Outline each blood parasite and name the species.
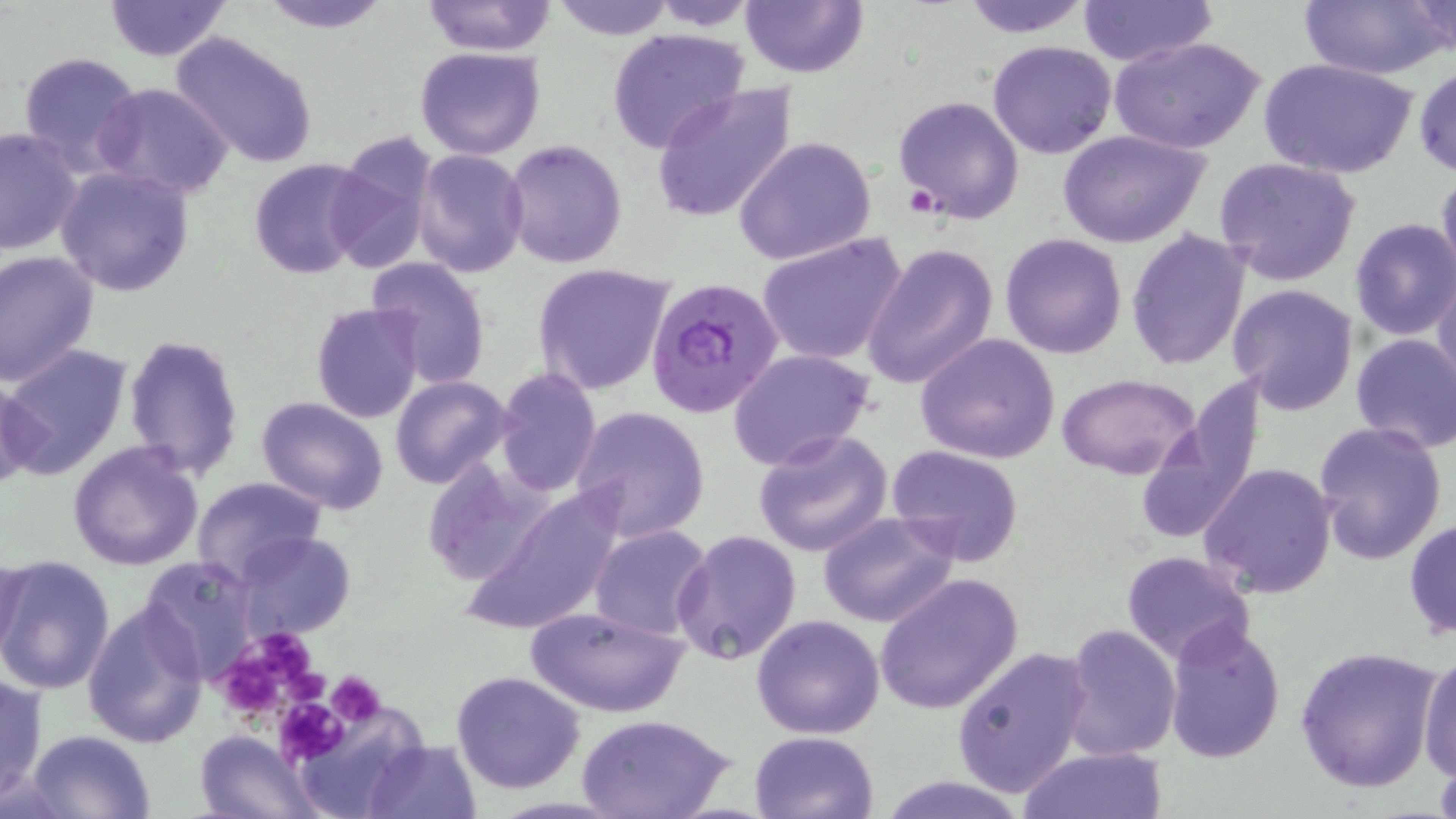

Approximate bounding boxes as [x1, y1, x2, y2] in pixels.
Plasmodium falciparum-infected red blood cells: [646, 277, 786, 418].
No Plasmodium ovale, Plasmodium malariae, Plasmodium vivax, Babesia divergens, or Trypanosoma brucei observed.

{
  "slide_level_diagnosis": "Plasmodium falciparum",
  "modality": "optical microscopy",
  "preparation": "thin blood film",
  "stain": "May-Grünwald-Giemsa",
  "magnification": "1000x",
  "field_of_view": "single",
  "platelet_locations": "approximate bounding boxes as [x1, y1, x2, y2] in pixels: [253, 631, 319, 684], [216, 654, 294, 719], [284, 666, 322, 711], [327, 671, 385, 724], [276, 696, 348, 764]",
  "image_size": "1456×819 pixels",
  "uninfected_red_blood_cell_locations": "approximate bounding boxes as [x1, y1, x2, y2] in pixels: [101, 0, 233, 60], [256, 0, 394, 33], [420, 0, 556, 57], [550, 0, 676, 38], [643, 0, 763, 30], [740, 0, 870, 78], [957, 0, 1094, 38], [1079, 0, 1217, 67], [1294, 0, 1452, 80], [1406, 1, 1454, 59], [606, 26, 749, 152], [170, 32, 319, 170], [1110, 35, 1266, 156], [986, 39, 1118, 159], [414, 46, 546, 162], [15, 51, 144, 175], [1258, 56, 1418, 181], [1414, 61, 1456, 181], [93, 82, 232, 199], [651, 84, 797, 224], [893, 94, 1025, 224], [0, 127, 84, 257], [1058, 128, 1211, 249], [733, 135, 879, 266], [325, 136, 441, 273], [502, 138, 630, 269], [412, 149, 529, 277], [1213, 156, 1362, 285], [248, 159, 373, 279], [55, 166, 194, 297], [1435, 169, 1456, 292], [1349, 218, 1456, 341], [1126, 228, 1251, 372], [756, 232, 907, 366], [1000, 233, 1128, 358], [861, 242, 997, 390], [0, 252, 99, 388], [366, 257, 492, 389], [532, 262, 675, 396], [1433, 266, 1456, 395], [1228, 283, 1360, 414], [311, 303, 424, 424], [916, 332, 1062, 464], [122, 333, 245, 480], [1350, 333, 1456, 454], [0, 344, 132, 481], [727, 347, 875, 472], [493, 367, 602, 498], [1055, 371, 1202, 478], [0, 376, 40, 493], [390, 376, 512, 489], [254, 397, 389, 515], [570, 405, 711, 541], [1310, 420, 1445, 565], [752, 427, 895, 557], [67, 441, 205, 571], [886, 445, 1025, 567], [424, 459, 548, 588], [1199, 462, 1338, 598], [191, 476, 328, 589], [461, 487, 626, 634], [816, 511, 959, 627], [1404, 517, 1456, 641], [589, 524, 713, 639], [673, 529, 802, 666], [233, 531, 356, 642], [1, 551, 26, 664], [1120, 551, 1256, 667], [0, 554, 116, 694], [137, 555, 258, 681], [873, 573, 1025, 715], [81, 598, 209, 749], [524, 603, 691, 718], [752, 613, 885, 738], [1163, 618, 1287, 765], [1062, 622, 1181, 760], [951, 644, 1094, 798], [1295, 645, 1444, 793], [1417, 651, 1456, 782], [451, 670, 585, 793], [0, 673, 48, 805], [577, 712, 734, 819], [26, 729, 154, 817], [749, 730, 878, 819], [194, 731, 320, 819], [361, 738, 482, 818], [1015, 746, 1169, 819], [881, 776, 1028, 819]"
}